Assess this cell for malaria.
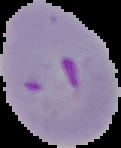
Parasitized.

Summary:
  - Image size: 121×148 pixels
  - Image type: cell region segmented out of the field of view; surrounding area masked to black
  - Preparation: thin blood film